Identify the parasite.
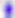

Toxoplasma gondii.

Photomicrograph. 400x magnification.